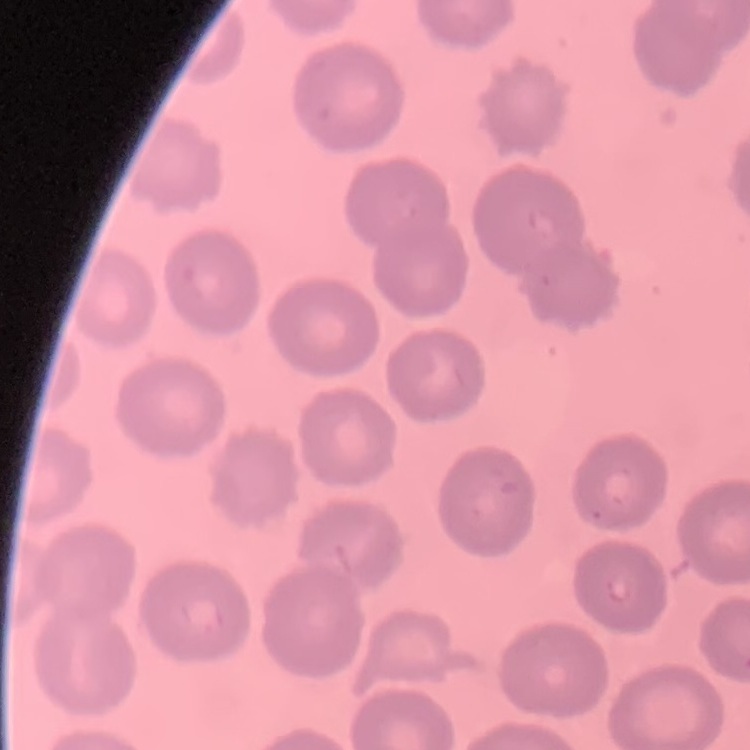
Summary:
  - Red blood cell morphology: no rouleaux formation
  - Stain: Field's or Giemsa
  - Image type: one tile cut from a larger photomicrograph
  - Preparation: thin blood film